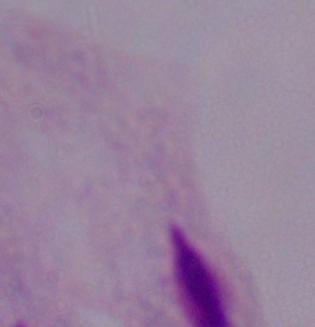

{
  "identification": "trichomonad",
  "magnification": "1000x",
  "modality": "photomicrograph"
}